Name the parasite shown.
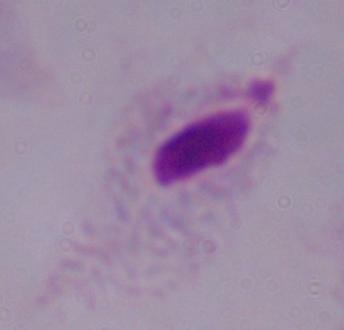
A trichomonad.

magnification = 1000x
modality = photomicrograph